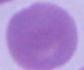
magnification: 1000x
identification: red blood cell
modality: photomicrograph